Identify the preparation type.
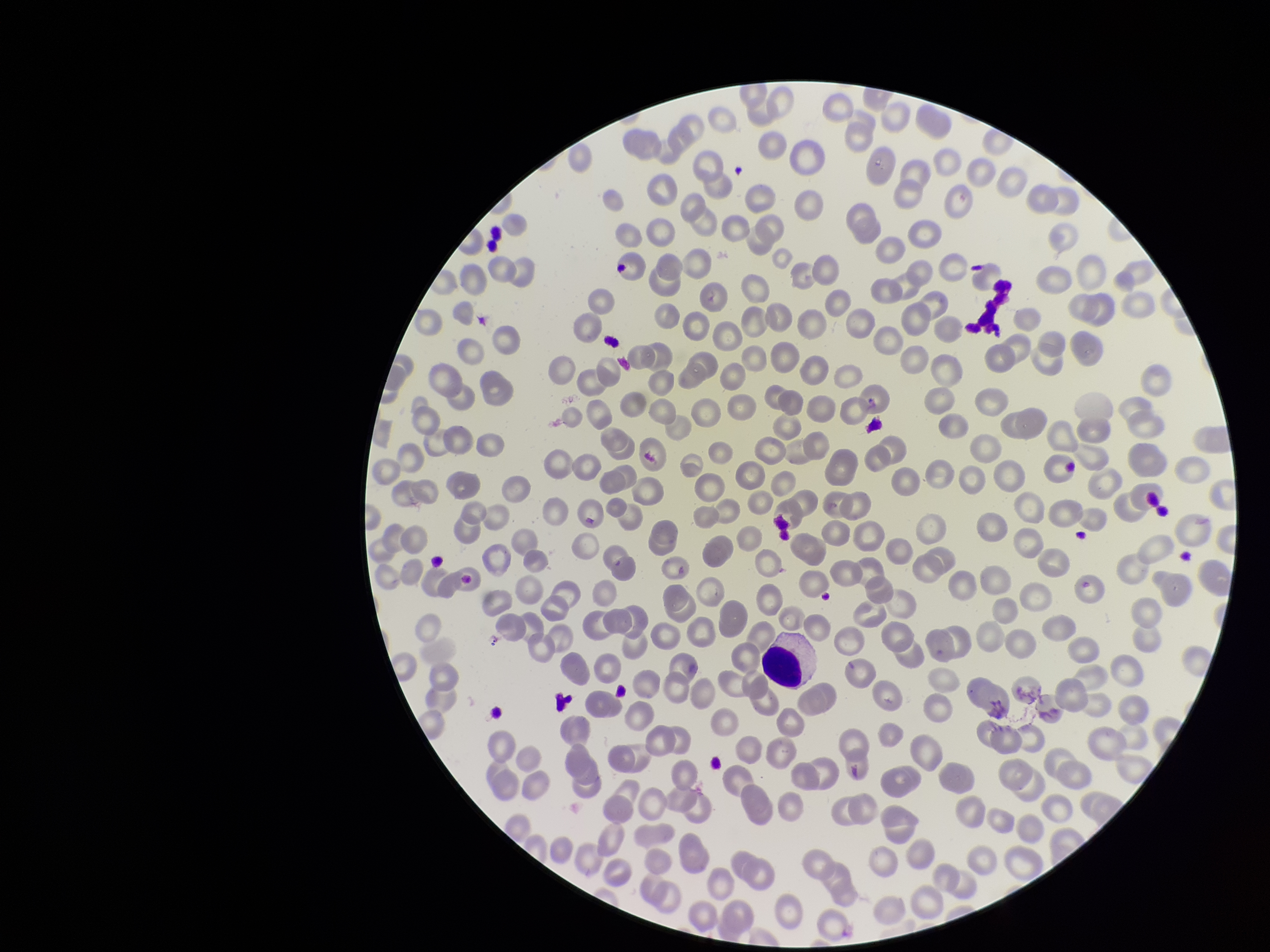

It is a thin blood smear.

Image is 1270×952 pixels. Smartphone photograph taken through the eyepiece of a microscope. Stained with Giemsa. Patient malaria status: negative. Single field of view. Parasitized red blood cells: none detected. Parasitized red blood cell count: 0. Red blood cell count: 248.